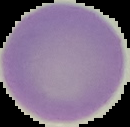

The area outside the segmented cell region is set to black. Malaria status: uninfected. Image is 130×127 pixels. From a thin blood smear.